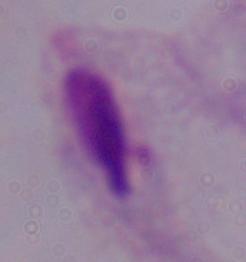
1000x magnification. Photomicrograph. A trichomonad is seen.